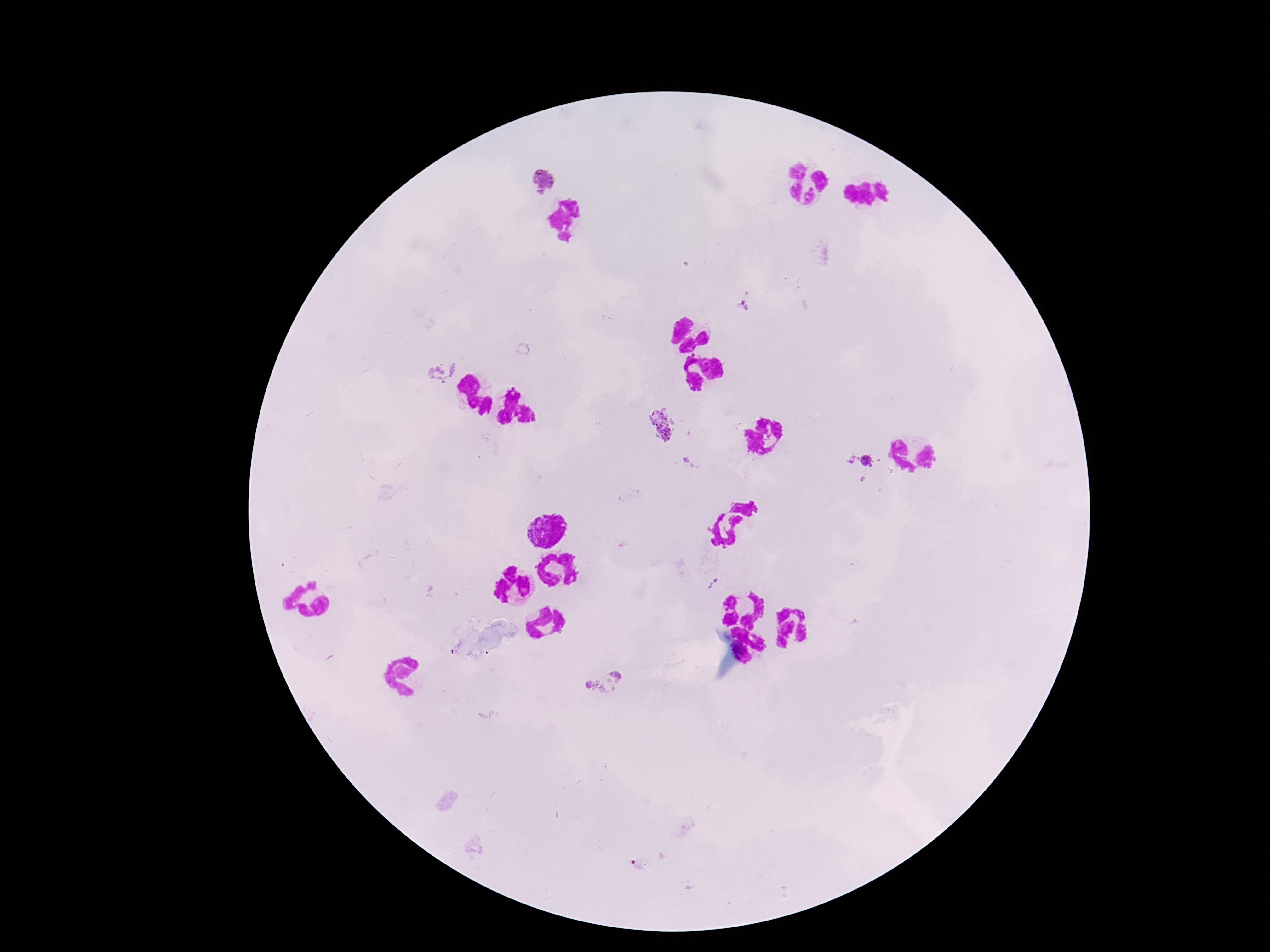

image size = 1270×952 pixels
patient malaria status = positive
preparation = thick peripheral-blood smear
field of view = one from this slide
capture = smartphone camera through the microscope eyepiece
Plasmodium parasite locations = approximate centers as (x, y) in pixels: (541, 179), (746, 306), (442, 368), (659, 424), (849, 458), (868, 461), (691, 463), (712, 583), (604, 681)
stain = Giemsa
magnification = 100x